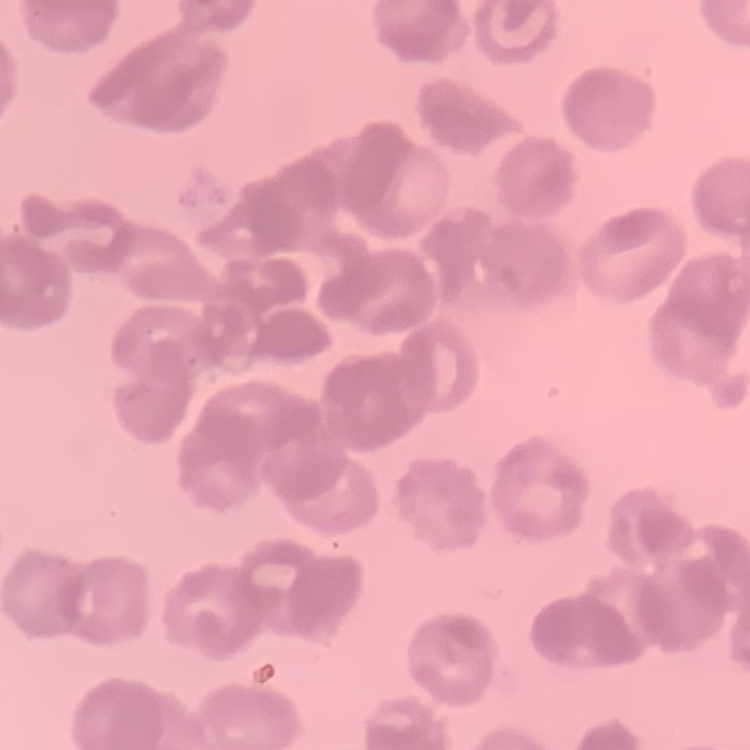
The erythrocytes exhibit rouleaux formation. Thin peripheral smear. One tile cut from a larger photomicrograph. Field's or Giemsa stain.